Name the blood parasite species.
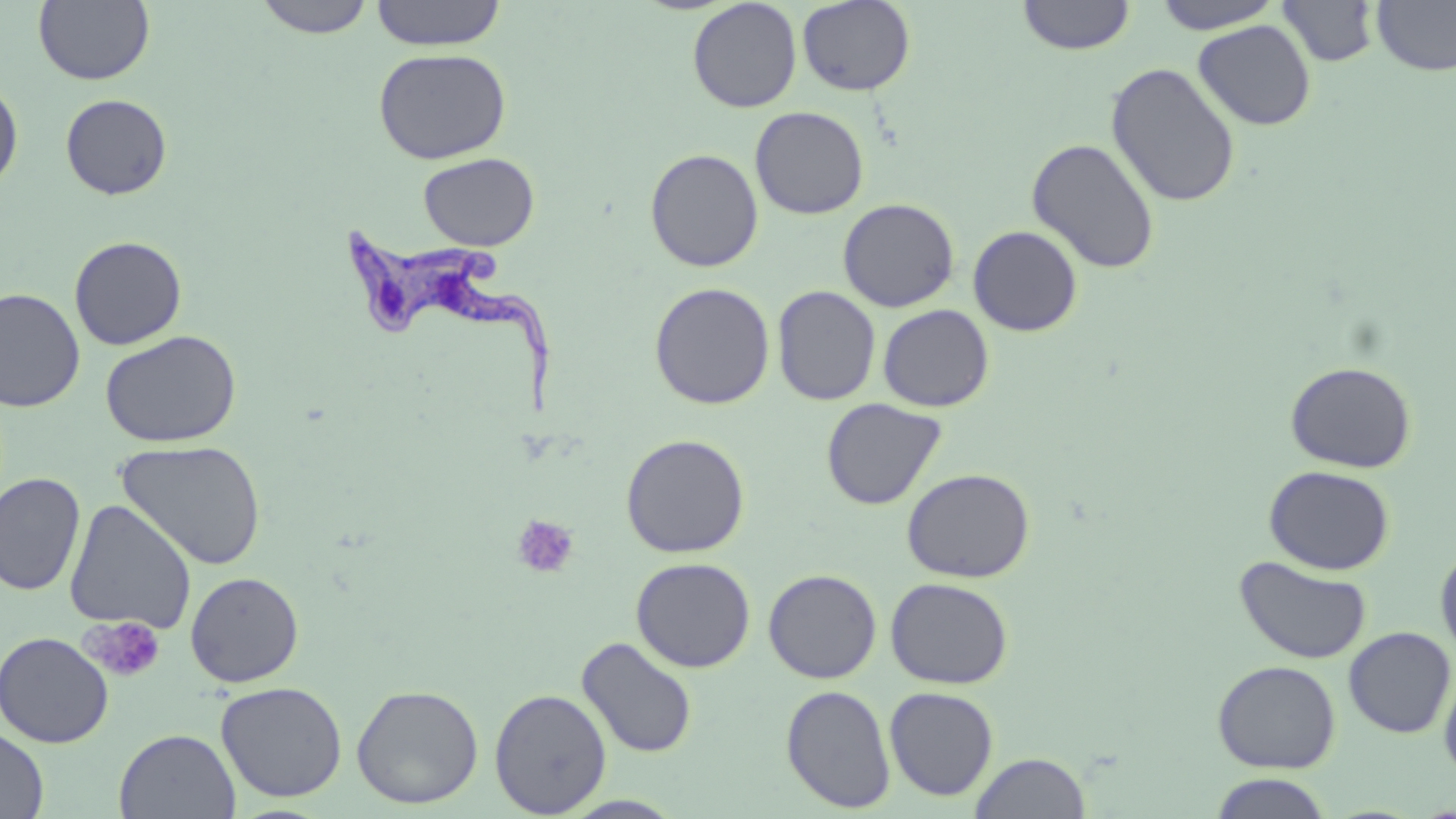

Trypanosoma brucei.

{
  "image_size": "1456×819 pixels",
  "magnification": "1000x",
  "field_of_view": "one of a larger specimen",
  "uninfected_red_blood_cell_locations": "approximate bounding boxes as (x1,y1)-(x2,y2) corner pairs in pixels: (253,0)-(376,38), (371,0)-(506,50), (797,0)-(916,96), (1017,0)-(1135,55), (1151,0)-(1285,34), (1276,0)-(1381,68), (1371,0)-(1456,76), (33,1)-(155,86), (687,1)-(802,113), (1193,20)-(1316,131), (373,48)-(511,164), (1106,62)-(1241,208), (0,77)-(24,196), (60,94)-(172,200), (750,106)-(869,219), (1026,138)-(1161,274), (644,148)-(764,272), (418,152)-(540,251), (838,198)-(959,312), (967,225)-(1083,337), (69,235)-(187,350), (649,281)-(775,410), (772,285)-(881,406), (0,288)-(86,412), (877,304)-(994,412), (100,329)-(242,448), (1285,360)-(1417,473), (821,398)-(947,510), (620,433)-(750,558), (117,439)-(268,570), (1264,465)-(1395,575), (901,467)-(1035,582), (0,471)-(85,596), (64,500)-(197,634), (1435,542)-(1456,663), (1235,554)-(1372,665), (631,557)-(756,672), (763,569)-(882,683), (185,571)-(304,687), (885,577)-(1013,689), (1343,626)-(1455,738), (0,631)-(114,748), (576,636)-(698,759), (1212,660)-(1341,773), (1439,665)-(1456,783), (215,681)-(348,802), (351,683)-(484,809), (781,684)-(897,813), (884,686)-(999,801), (489,688)-(612,816), (0,726)-(49,818), (114,728)-(241,818), (969,751)-(1091,818), (1207,773)-(1335,818), (558,794)-(687,818)",
  "platelet_locations": "approximate bounding boxes as (x1,y1)-(x2,y2) corner pairs in pixels: (511,514)-(580,579), (82,616)-(166,682)",
  "modality": "optical microscopy",
  "trypanosoma_brucei_locations": "approximate bounding boxes as (x1,y1)-(x2,y2) corner pairs in pixels: (337,226)-(560,426)",
  "preparation": "thin blood film",
  "stain": "May-Grünwald-Giemsa"
}